Report the malaria status of this cell.
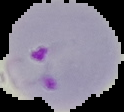
Parasitized.

Summary:
  - Image type: segmented cell region with the area outside set to black
  - Image size: 124×112 pixels
  - Preparation: thin blood smear